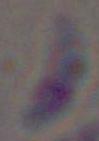

1000x magnification. Toxoplasma gondii is seen. Photomicrograph.